Identify the preparation type.
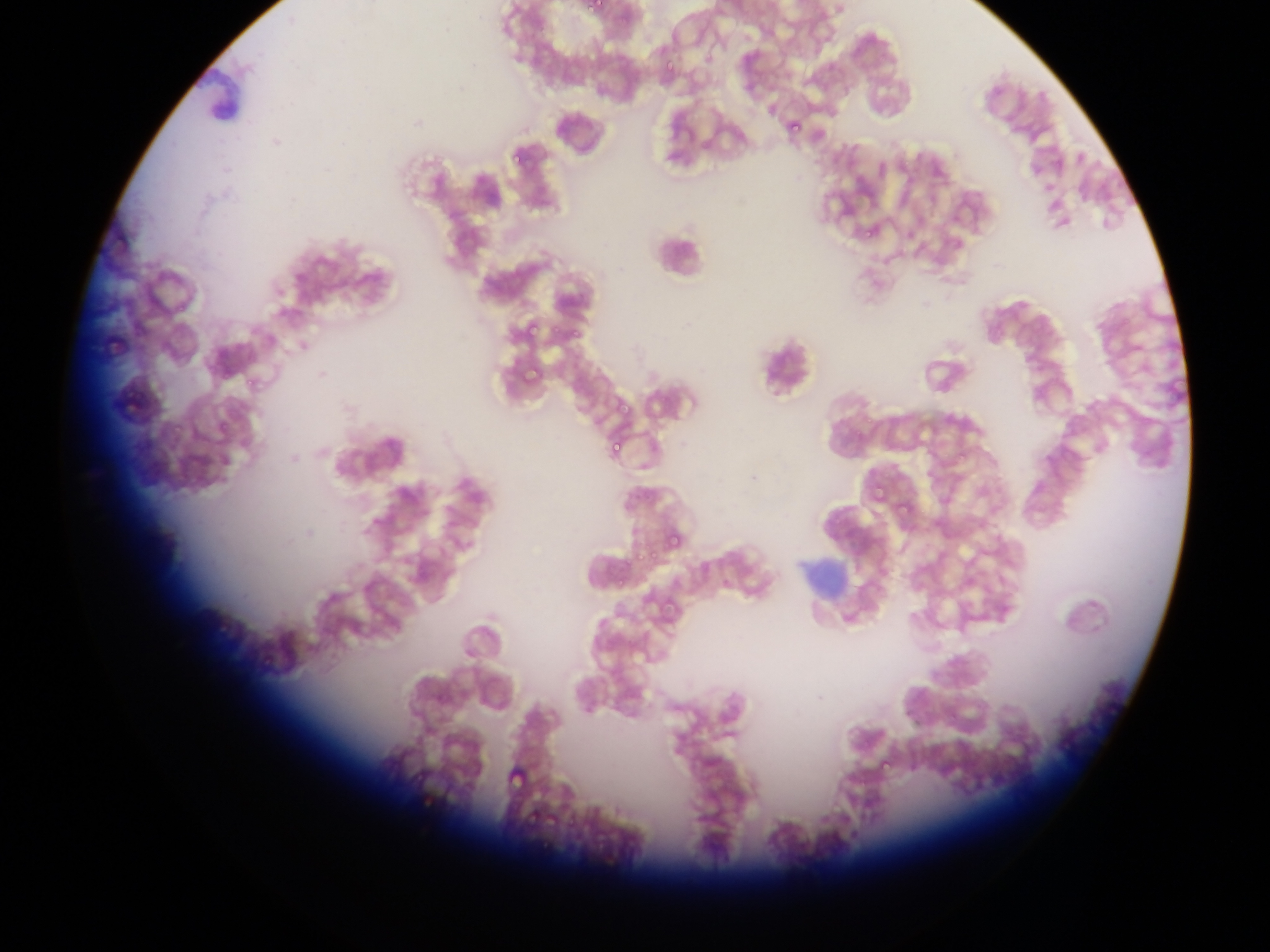
This is a thin smear.

Approximate bounding boxes as left top right bottom in pixels. Malaria parasite locations: 588 0 603 14; 661 40 680 81; 788 118 803 132; 509 150 527 167; 1073 151 1086 166; 857 223 875 239; 522 315 542 339; 562 321 590 343; 520 359 546 385; 113 372 150 424; 242 379 259 395; 614 403 634 415; 165 418 195 438; 214 419 235 439; 604 434 628 455; 864 482 890 509; 897 498 911 514; 665 519 693 553; 634 545 651 562; 610 575 636 592; 503 754 532 792; 881 757 896 774; 418 790 436 813; 527 812 539 830; 541 813 564 832; 535 841 557 858. Photographed through a microscope with a mobile-phone camera. Single field of view. Collected in Ghana. Image is 1270×952 pixels.